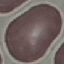
Result: negative for malaria parasites. Thin blood smear. Giemsa-stained preparation. Acquired by smartphone through the microscope eyepiece. Cell patch, automatically extracted from a larger field of view and resized to 64 × 64 pixels.